Classify this cell by malaria status.
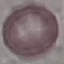

Uninfected.

Photographed with a smartphone camera at the microscope eyepiece. Giemsa stain. Thin smear of blood. Cell patch, automatically extracted from a larger field of view and resized to 64 × 64 pixels.